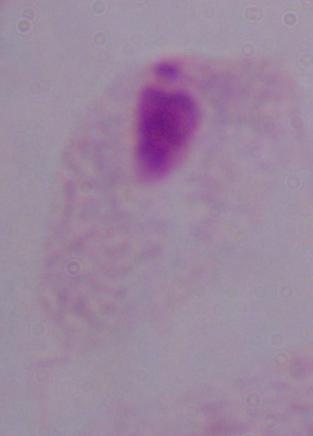

Summary:
  - Identification: trichomonad
  - Magnification: 1000x
  - Modality: photomicrograph